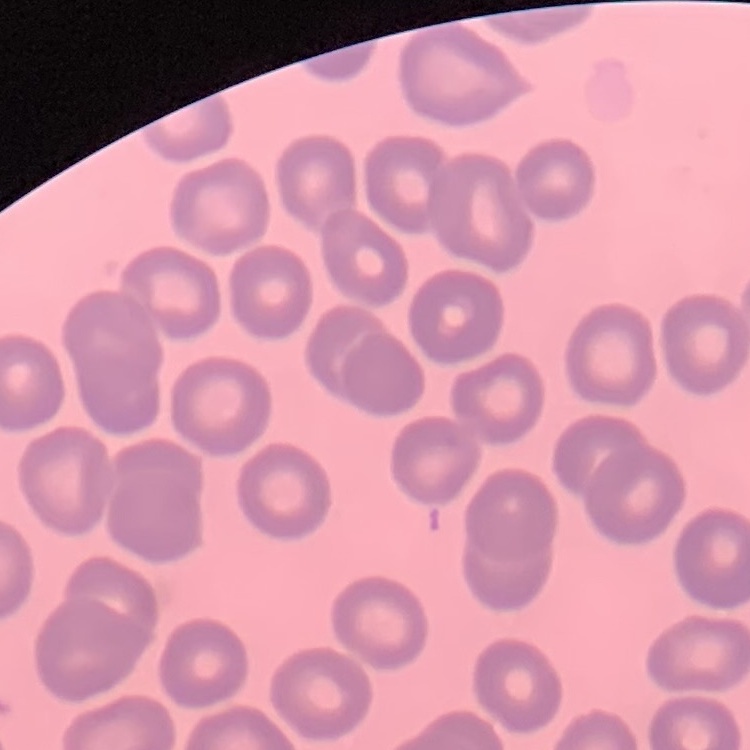
Summary:
  - Red blood cell morphology: no rouleaux formation
  - Stain: Field's or Giemsa
  - Image type: one tile cut from a larger photomicrograph
  - Preparation: thin peripheral smear